State which parasite is depicted.
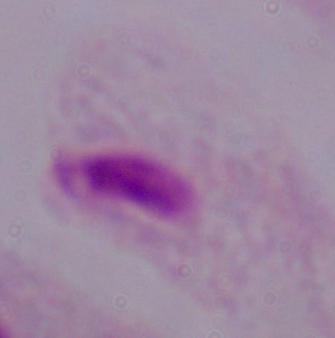
A trichomonad.

1000x magnification. Micrograph.